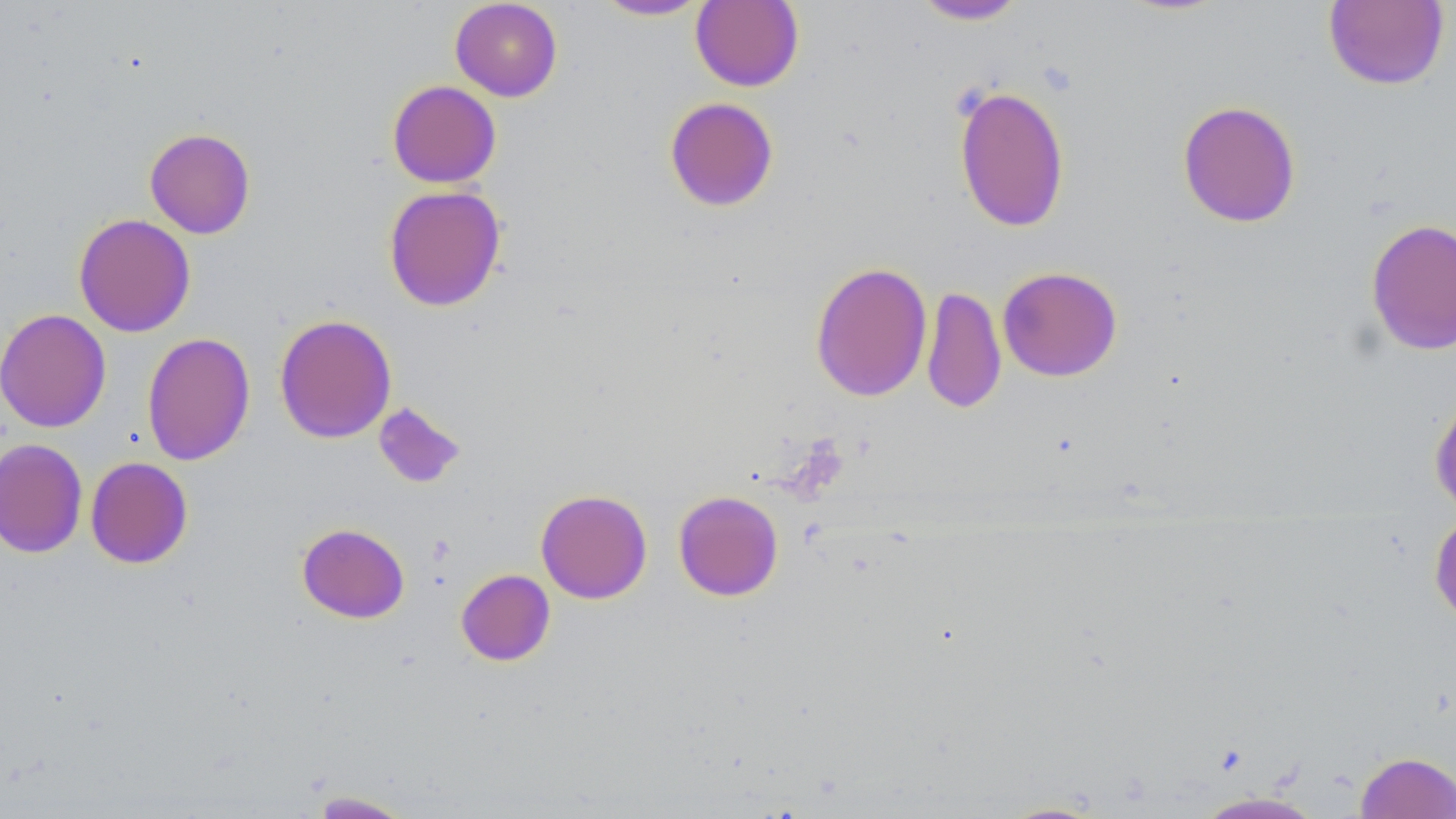
Summary:
  - Coordinate format: approximate bounding boxes as (x1, y1, x2, y2) in pixels
  - Uninfected red blood cell locations: (449, 0, 563, 102), (911, 0, 1028, 25), (592, 1, 712, 21), (690, 1, 804, 92), (1323, 1, 1450, 90), (386, 80, 501, 188), (953, 85, 1070, 232), (664, 97, 779, 212), (1177, 100, 1301, 228), (144, 128, 256, 239), (383, 184, 507, 312), (73, 213, 196, 337), (1365, 217, 1456, 355), (809, 261, 932, 402), (997, 266, 1123, 381), (921, 285, 1006, 414), (0, 308, 111, 433), (274, 313, 397, 444), (141, 332, 255, 466), (1429, 391, 1456, 519), (372, 401, 466, 489), (0, 438, 88, 558), (85, 456, 193, 569), (535, 488, 653, 604), (673, 490, 784, 601), (1429, 511, 1456, 626), (296, 523, 410, 624), (456, 569, 556, 666), (1355, 751, 1456, 818), (306, 790, 416, 818), (1192, 791, 1328, 819), (993, 800, 1110, 818)
  - Slide-level diagnosis: no evidence of blood parasites
  - Preparation: thin blood film
  - Stain: May-Grünwald-Giemsa
  - Field of view: one of a larger specimen
  - Magnification: 1000x
  - Image size: 1456×819 pixels
  - Modality: optical microscopy